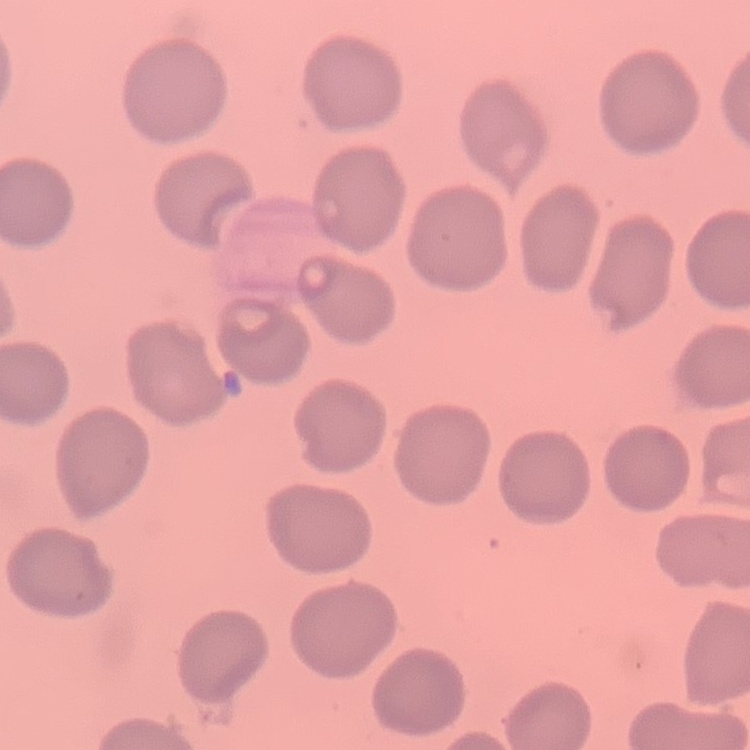

The erythrocytes show no rouleaux formation. Stained with either Field's or Giemsa. One tile cut from a larger photomicrograph. Thin peripheral smear.